Assess this cell for malaria.
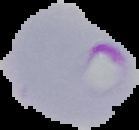
It is parasitized.

{
  "preparation": "thin blood smear",
  "image_size": "139×130 pixels",
  "image_type": "cell region segmented out of the field of view; surrounding area masked to black"
}